Name the blood parasite species.
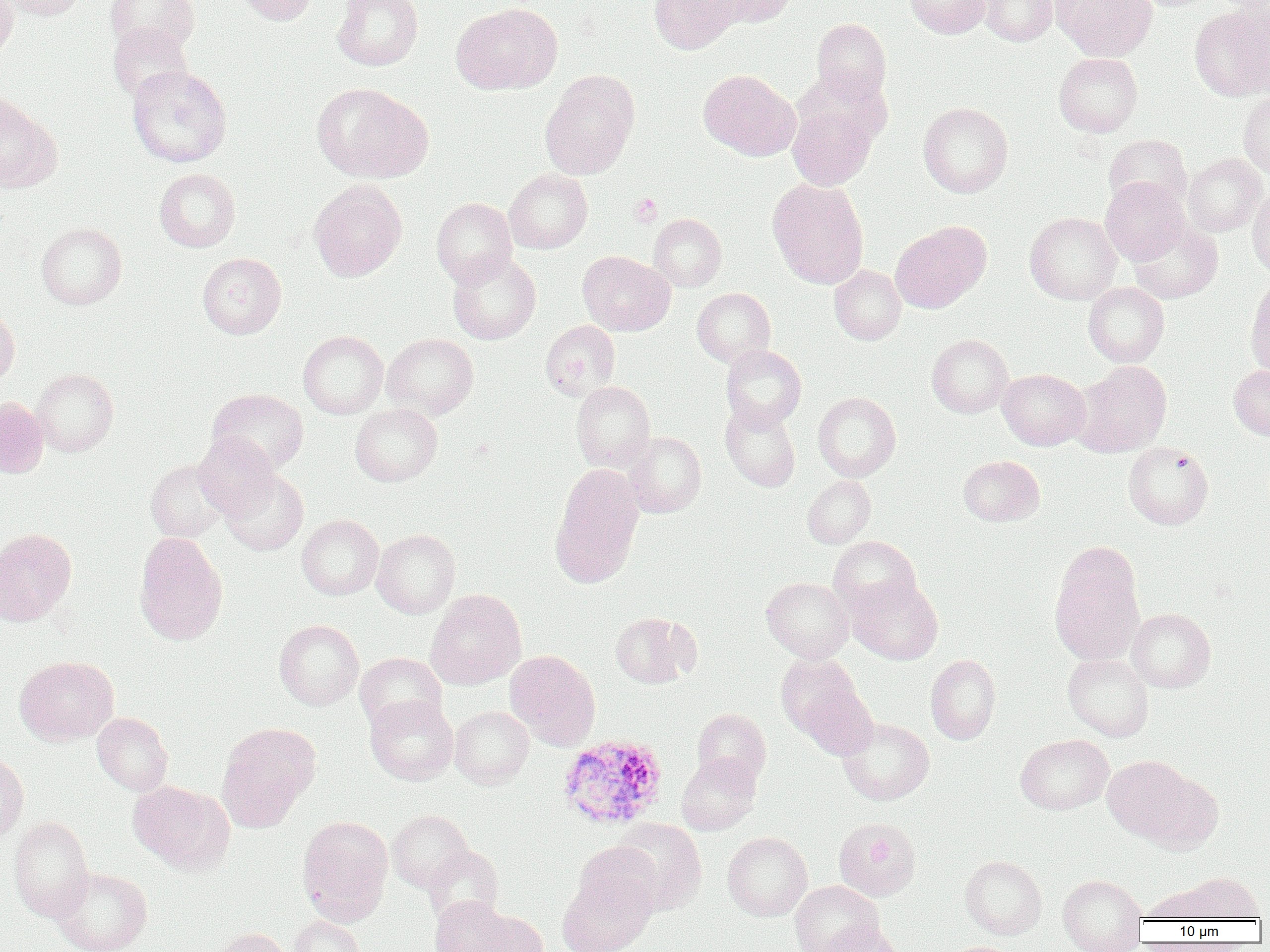
Plasmodium ovale.

Summary:
  - Coordinate format: approximate bounding boxes as [x1, y1, x2, y2] in pixels
  - Uninfected red blood cell locations: [0, 0, 18, 62], [2, 0, 87, 21], [106, 0, 199, 56], [231, 0, 319, 25], [332, 0, 423, 70], [649, 0, 744, 55], [710, 0, 797, 27], [905, 0, 991, 38], [980, 0, 1058, 46], [1051, 0, 1157, 61], [451, 3, 561, 95], [1189, 6, 1270, 101], [812, 18, 891, 103], [108, 23, 192, 101], [1054, 52, 1142, 136], [126, 64, 231, 167], [698, 69, 799, 160], [541, 70, 639, 180], [312, 83, 432, 182], [1239, 90, 1270, 178], [0, 93, 59, 193], [787, 102, 876, 190], [918, 102, 1013, 197], [1104, 134, 1192, 208], [1184, 154, 1267, 236], [154, 168, 241, 252], [504, 169, 592, 253], [767, 177, 869, 289], [1100, 177, 1188, 265], [309, 178, 407, 282], [1247, 186, 1270, 276], [431, 198, 517, 285], [1024, 212, 1122, 305], [649, 214, 727, 291], [1128, 220, 1222, 303], [35, 222, 126, 310], [890, 222, 990, 313], [447, 251, 541, 344], [578, 251, 675, 336], [197, 252, 286, 339], [829, 265, 906, 344], [1245, 278, 1270, 380], [1083, 281, 1169, 367], [692, 288, 775, 366], [0, 303, 19, 387], [540, 320, 620, 401], [298, 331, 388, 419], [382, 333, 478, 419], [927, 334, 1014, 418], [721, 344, 806, 430], [1072, 360, 1172, 457], [1229, 365, 1270, 440], [31, 368, 118, 457], [997, 369, 1090, 450], [571, 381, 655, 471], [208, 388, 308, 473], [813, 391, 901, 481], [0, 397, 48, 478], [720, 402, 800, 491], [350, 404, 442, 486], [623, 432, 706, 518], [194, 433, 280, 517], [1123, 442, 1213, 529], [959, 455, 1044, 526], [146, 459, 230, 543], [550, 465, 644, 588], [220, 468, 308, 555], [803, 476, 875, 548], [297, 514, 383, 600], [0, 528, 76, 624], [371, 528, 460, 618], [134, 532, 228, 645], [828, 535, 921, 616], [1050, 553, 1145, 666], [761, 577, 853, 662], [847, 577, 943, 664], [425, 589, 526, 690], [1127, 608, 1215, 692], [609, 611, 697, 688], [274, 619, 363, 710], [505, 650, 601, 750], [776, 651, 870, 745], [354, 652, 447, 734], [1063, 653, 1154, 742], [926, 654, 1000, 744], [15, 656, 118, 745], [364, 695, 458, 784], [449, 706, 534, 788], [692, 708, 771, 787], [92, 712, 173, 796], [838, 717, 934, 804], [217, 723, 319, 831], [1015, 734, 1113, 815], [676, 753, 761, 835], [0, 754, 28, 842], [1101, 755, 1199, 843], [1141, 772, 1223, 853], [128, 780, 234, 874], [387, 810, 472, 892], [297, 815, 393, 924], [8, 816, 94, 921], [610, 818, 707, 914], [834, 818, 921, 902], [723, 831, 812, 921], [572, 840, 664, 918], [423, 845, 504, 925], [960, 855, 1046, 939], [52, 866, 152, 952], [1182, 872, 1263, 922], [557, 873, 656, 952], [1058, 875, 1147, 951], [789, 880, 884, 952], [1142, 884, 1223, 923], [431, 895, 511, 952], [468, 909, 549, 952], [290, 915, 365, 952], [816, 922, 904, 952], [212, 927, 294, 952]
  - Plasmodium ovale-infected red blood cell locations: [557, 734, 668, 829]
  - Platelet locations: [630, 193, 662, 225]
  - Field of view: one of a larger specimen
  - Magnification: 1000x
  - Preparation: thin blood smear
  - Modality: light microscopy
  - Image size: 1270×952 pixels